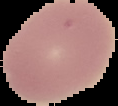

preparation = thin blood film
image size = 118×106 pixels
image type = cell region segmented out of the field of view; surrounding area masked to black
malaria status = uninfected